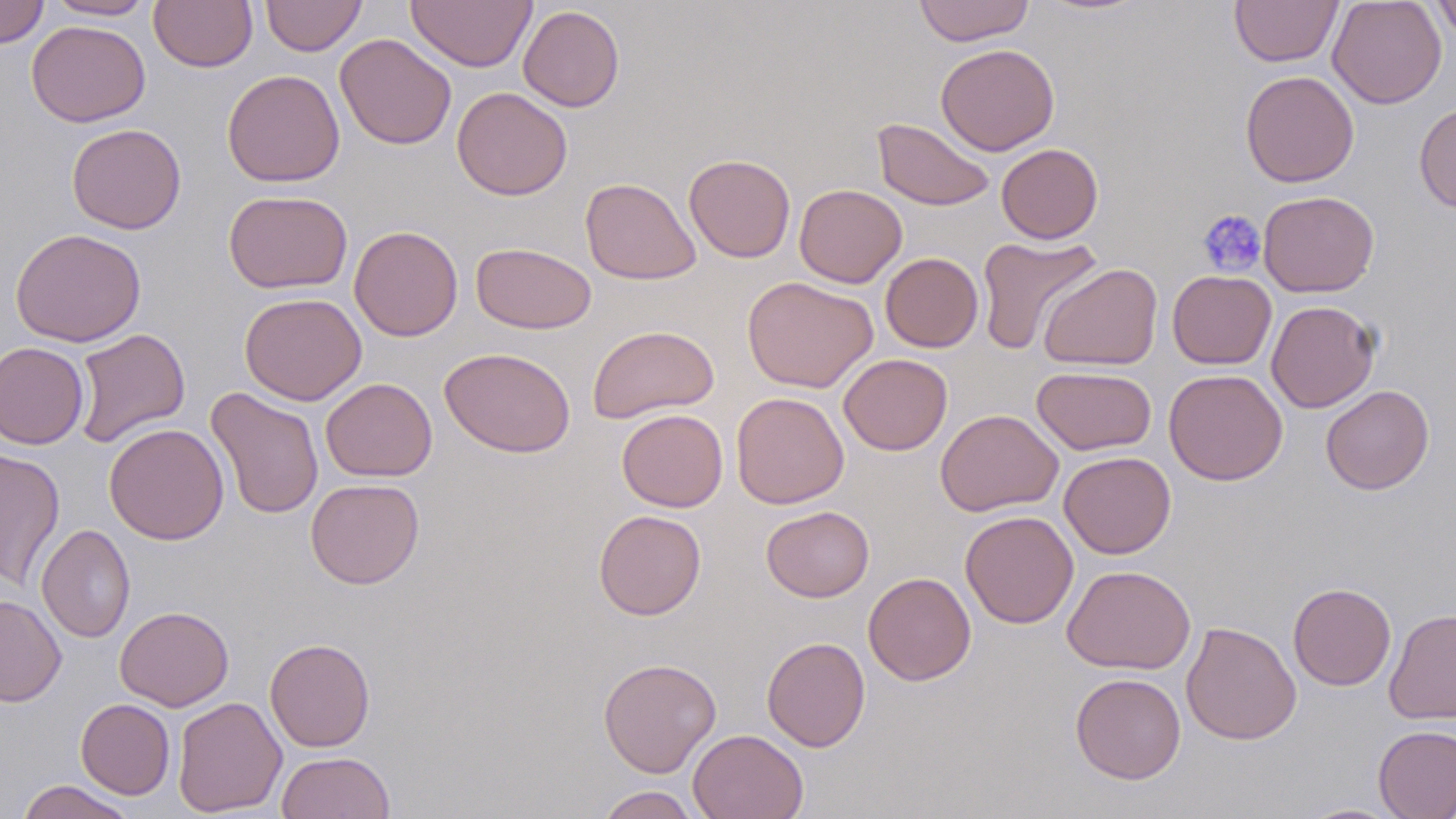
Summary:
  - Coordinate format: approximate bounding boxes as (x1, y1, x2, y2) in pixels
  - Uninfected red blood cell locations: (0, 0, 49, 49), (45, 0, 155, 20), (149, 0, 258, 72), (261, 0, 366, 56), (406, 0, 537, 72), (914, 0, 1035, 46), (1229, 0, 1343, 67), (1327, 0, 1447, 109), (1432, 0, 1456, 45), (518, 5, 625, 111), (26, 20, 150, 127), (334, 33, 457, 150), (935, 43, 1060, 155), (222, 69, 345, 187), (1240, 70, 1359, 187), (451, 86, 572, 200), (1414, 102, 1456, 213), (871, 118, 995, 211), (66, 123, 186, 234), (996, 143, 1103, 244), (684, 154, 796, 263), (579, 177, 700, 285), (794, 184, 907, 288), (223, 189, 353, 294), (1258, 190, 1379, 297), (349, 225, 463, 341), (9, 228, 146, 348), (975, 234, 1102, 355), (470, 242, 597, 334), (880, 252, 983, 353), (1038, 262, 1163, 370), (1167, 270, 1276, 369), (742, 276, 879, 393), (239, 292, 367, 406), (1266, 300, 1380, 413), (588, 324, 719, 424), (73, 328, 191, 447), (0, 342, 88, 449), (439, 347, 576, 457), (838, 353, 953, 455), (1032, 365, 1156, 456), (1163, 369, 1288, 486), (320, 378, 437, 481), (1321, 385, 1434, 495), (206, 387, 324, 520), (731, 392, 849, 508), (616, 409, 728, 512), (935, 409, 1063, 516), (104, 423, 229, 544), (0, 448, 65, 590), (1059, 451, 1176, 559), (305, 478, 425, 589), (761, 505, 874, 602), (593, 509, 706, 620), (960, 510, 1079, 628), (36, 524, 135, 643), (1061, 565, 1196, 675), (863, 571, 976, 685), (1288, 583, 1396, 691), (0, 593, 66, 707), (115, 605, 234, 711), (1384, 607, 1456, 725), (1181, 621, 1301, 745), (762, 636, 870, 751), (264, 637, 376, 752), (597, 658, 721, 778), (1070, 672, 1186, 784), (172, 696, 287, 817), (75, 699, 175, 799), (1373, 724, 1456, 819), (688, 728, 809, 819), (276, 751, 395, 818), (17, 780, 138, 819), (593, 786, 702, 819), (1296, 803, 1406, 818)
  - Platelet locations: (1196, 208, 1267, 278)
  - Slide-level diagnosis: negative for blood parasites
  - Preparation: thin blood smear
  - Image size: 1456×819 pixels
  - Magnification: 1000x
  - Stain: May-Grünwald-Giemsa
  - Modality: optical microscopy
  - Field of view: one of a larger specimen